Classify this cell by malaria status.
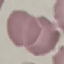
Uninfected.

{
  "image_type": "automatically extracted cell patch, resized to 64 × 64 pixels",
  "capture": "smartphone through the microscope eyepiece",
  "stain": "Giemsa",
  "preparation": "thin smear"
}